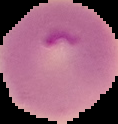

image type = segmented cell region with the area outside set to black
image size = 118×124 pixels
result = malaria parasites identified
preparation = thin blood smear